Look for Plasmodium parasites.
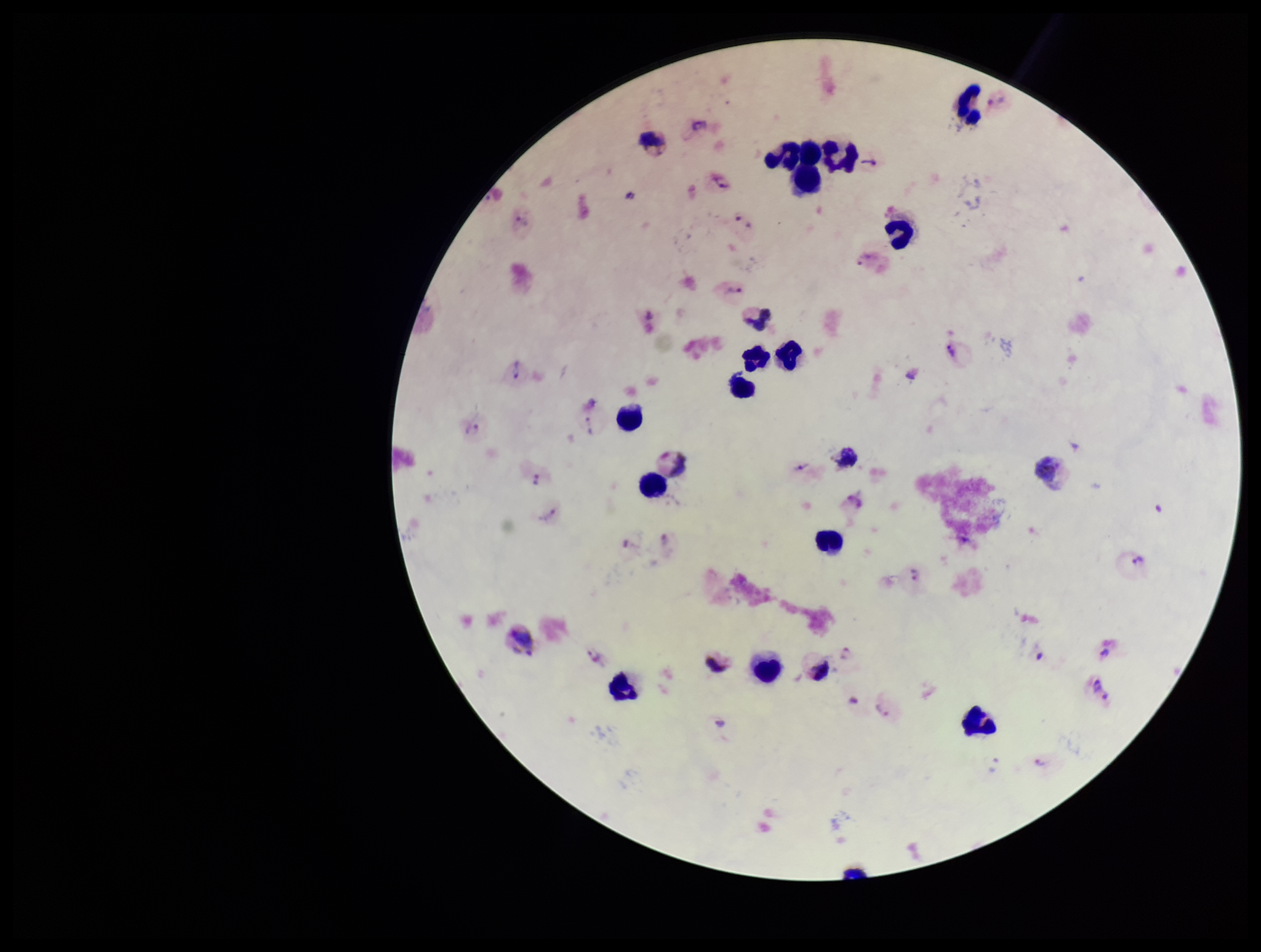
Detected.

species reported for this patient = Plasmodium vivax
patient malaria status = infected
capture = smartphone photograph through the microscope eyepiece
stain = Giemsa
parasite count = 26
image size = 1261×952 pixels
preparation = thick blood smear
field of view = one from this slide
leukocyte count = 21